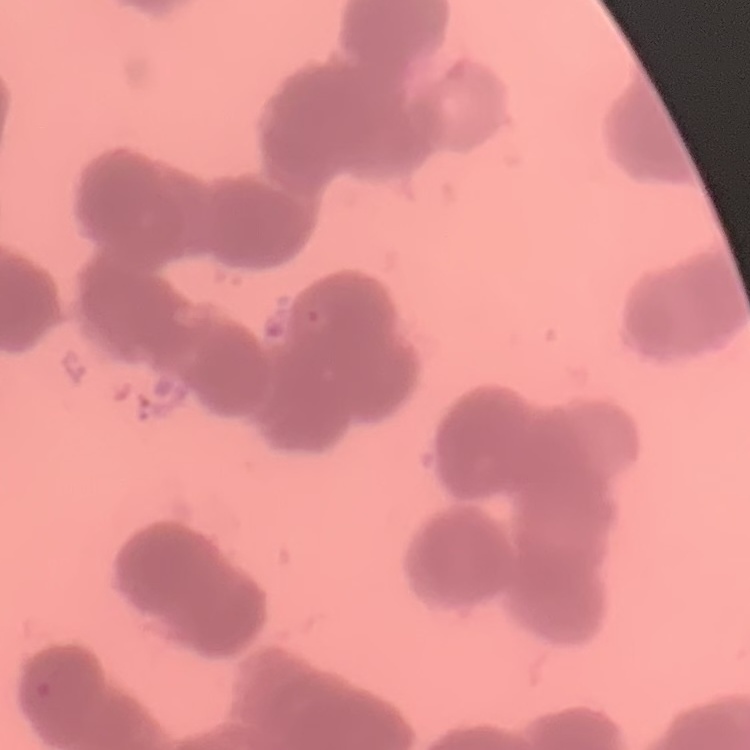 The erythrocytes exhibit rouleaux formation. Square crop of a larger photomicrograph. Thin peripheral smear. Stained with either Field's or Giemsa.